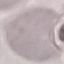
Malaria status: uninfected. Giemsa stain. Acquired by smartphone through the microscope eyepiece. Thin blood film. Automatically extracted cell patch, resized to 64 × 64 pixels.